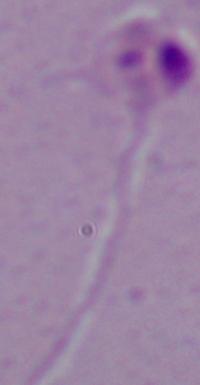

Summary:
  - Magnification: 1000x
  - Modality: photomicrograph
  - Identification: Leishmania